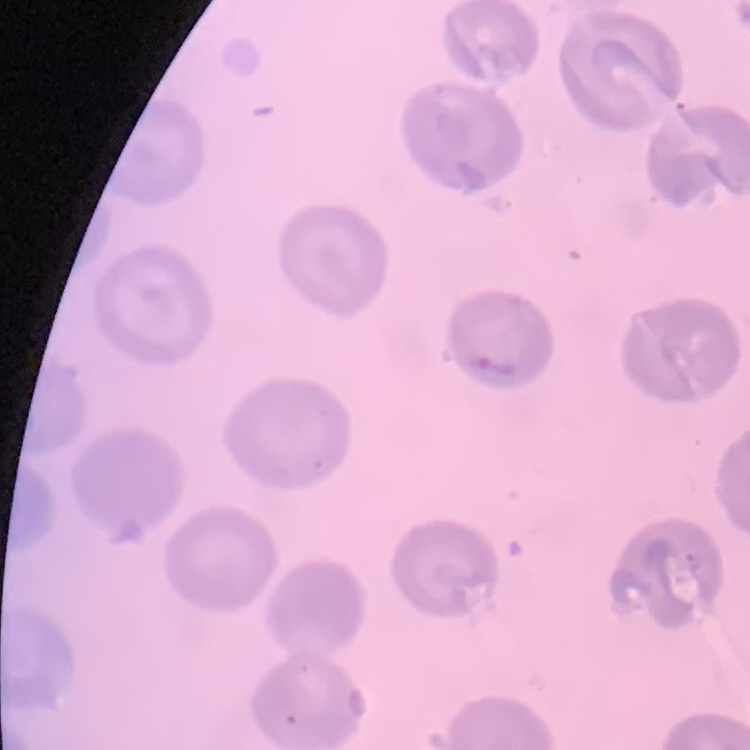
The red blood cells exhibit no rouleaux formation. One tile cut from a larger photomicrograph. Stained with either Field's or Giemsa. Thin blood smear.